Name the cell type shown.
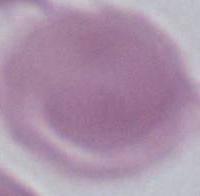
An erythrocyte.

{
  "magnification": "1000x",
  "modality": "photomicrograph"
}